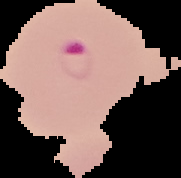
Result: malaria parasites identified. The area outside the segmented cell region is set to black. From a thin blood smear. Image is 181×178 pixels.